Identify the blood parasite species.
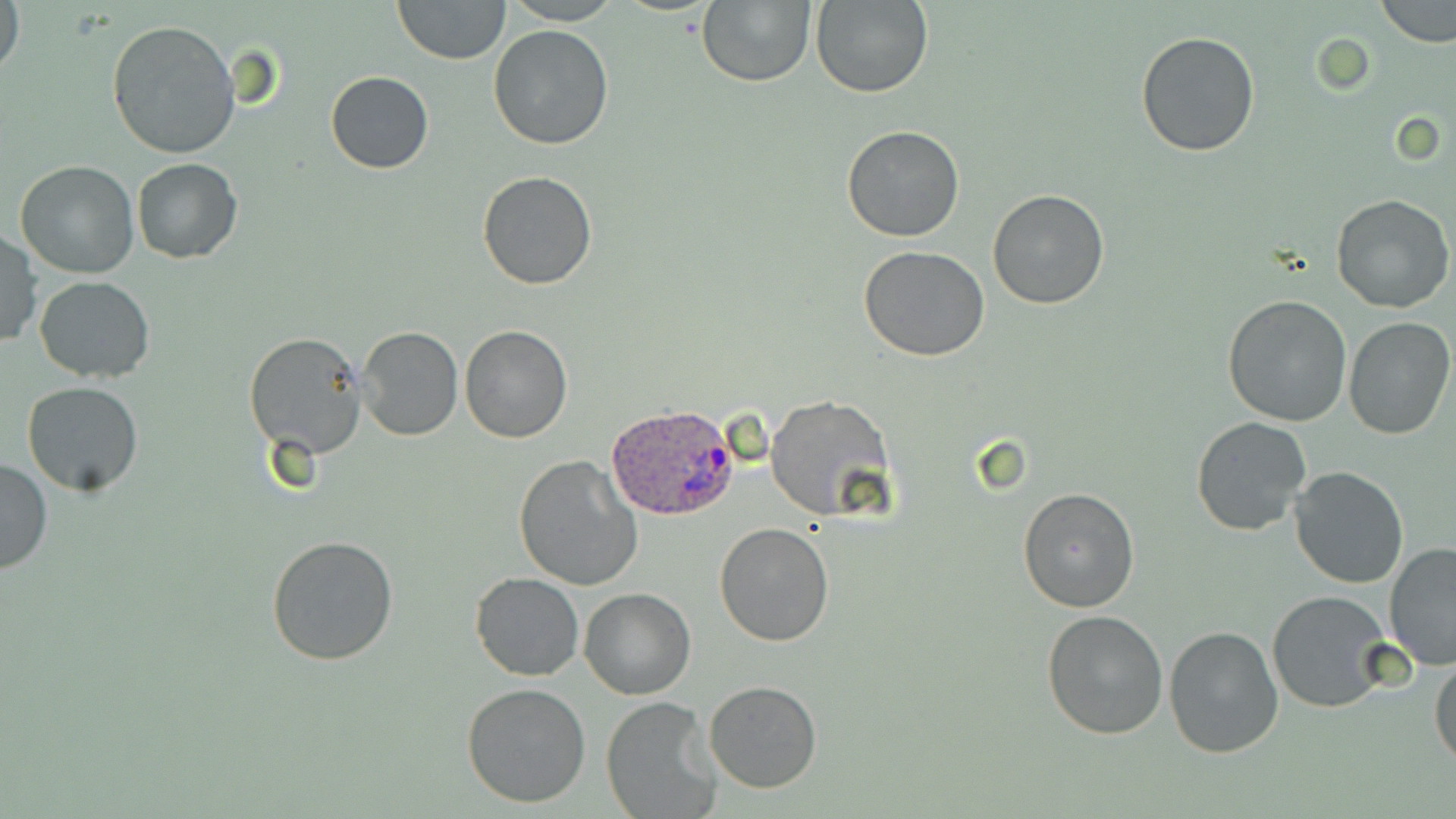

Plasmodium ovale.

Summary:
  - Coordinate format: approximate bounding boxes as named x1/y1/x2/y2 corners in pixels
  - Uninfected red blood cell locations: (x1=1, y1=0, x2=24, y2=83), (x1=392, y1=0, x2=511, y2=64), (x1=504, y1=0, x2=619, y2=24), (x1=696, y1=0, x2=816, y2=87), (x1=810, y1=0, x2=933, y2=98), (x1=1375, y1=0, x2=1455, y2=47), (x1=107, y1=20, x2=240, y2=159), (x1=487, y1=24, x2=615, y2=150), (x1=1134, y1=30, x2=1260, y2=159), (x1=326, y1=71, x2=434, y2=174), (x1=841, y1=124, x2=965, y2=242), (x1=131, y1=158, x2=242, y2=262), (x1=15, y1=161, x2=140, y2=279), (x1=478, y1=171, x2=598, y2=291), (x1=987, y1=190, x2=1110, y2=310), (x1=1331, y1=194, x2=1453, y2=314), (x1=0, y1=231, x2=41, y2=350), (x1=859, y1=246, x2=990, y2=363), (x1=34, y1=275, x2=157, y2=383), (x1=1221, y1=294, x2=1352, y2=428), (x1=1342, y1=316, x2=1455, y2=439), (x1=458, y1=324, x2=573, y2=443), (x1=357, y1=326, x2=462, y2=440), (x1=243, y1=332, x2=368, y2=460), (x1=22, y1=381, x2=143, y2=495), (x1=765, y1=394, x2=894, y2=522), (x1=1191, y1=417, x2=1312, y2=537), (x1=512, y1=455, x2=642, y2=593), (x1=0, y1=456, x2=52, y2=576), (x1=1289, y1=464, x2=1409, y2=589), (x1=1017, y1=486, x2=1142, y2=614), (x1=715, y1=522, x2=833, y2=646), (x1=266, y1=533, x2=400, y2=668), (x1=1382, y1=541, x2=1456, y2=669), (x1=470, y1=573, x2=584, y2=680), (x1=579, y1=587, x2=695, y2=701), (x1=1268, y1=591, x2=1395, y2=713), (x1=1041, y1=608, x2=1168, y2=741), (x1=1164, y1=626, x2=1285, y2=759), (x1=1430, y1=654, x2=1456, y2=771), (x1=703, y1=680, x2=823, y2=794), (x1=461, y1=682, x2=592, y2=808), (x1=601, y1=697, x2=720, y2=819)
  - Plasmodium ovale-infected red blood cell locations: (x1=605, y1=403, x2=738, y2=523)
  - Modality: light microscopy
  - Image size: 1456×819 pixels
  - Preparation: thin blood film
  - Stain: May-Grünwald-Giemsa
  - Field of view: single
  - Magnification: 1000x